Outline each uninfected red blood cell.
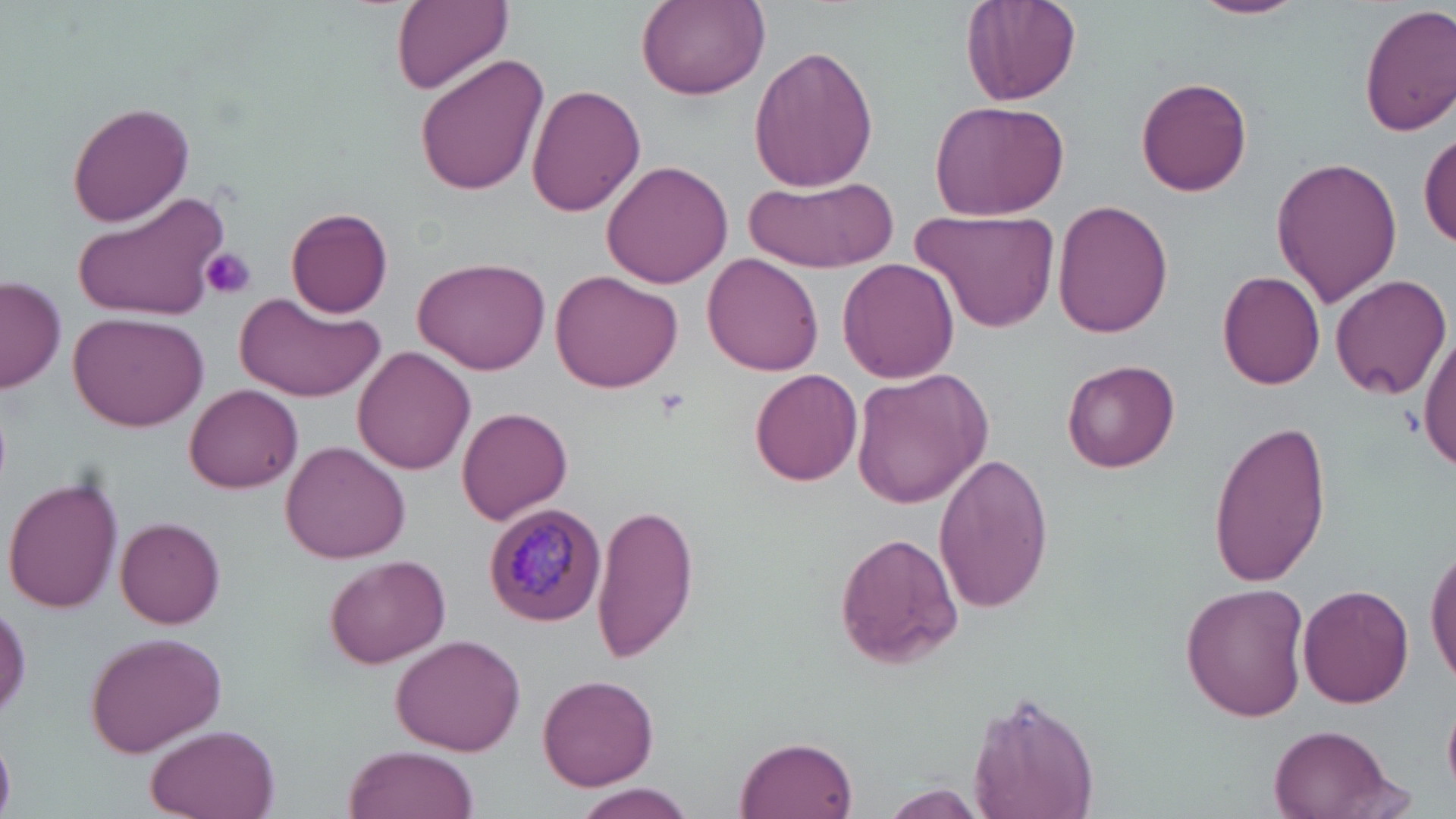

Approximate bounding boxes as (x1, y1, x2, y2) in pixels.
Uninfected red blood cells: (393, 0, 512, 92), (960, 0, 1082, 107), (1190, 0, 1307, 20), (635, 1, 769, 100), (1360, 4, 1456, 136), (747, 45, 879, 193), (414, 53, 549, 197), (1136, 77, 1253, 196), (527, 85, 646, 217), (927, 98, 1071, 221), (67, 102, 195, 227), (1418, 128, 1455, 250), (1271, 156, 1404, 308), (600, 158, 733, 290), (745, 174, 896, 273), (78, 190, 227, 321), (1054, 199, 1175, 338), (916, 207, 1060, 334), (284, 208, 393, 317), (703, 252, 824, 376), (415, 255, 551, 373), (838, 260, 960, 385), (550, 269, 683, 391), (1217, 271, 1326, 389), (1329, 272, 1452, 401), (0, 277, 65, 392), (240, 298, 384, 401), (66, 311, 208, 430), (1419, 330, 1456, 471), (354, 346, 475, 477), (1064, 359, 1180, 472), (751, 368, 862, 487), (853, 368, 990, 509), (185, 384, 303, 493), (458, 406, 571, 526), (1208, 417, 1331, 587), (281, 441, 410, 564), (935, 454, 1054, 613), (4, 475, 124, 615), (593, 504, 698, 659), (117, 515, 227, 628), (836, 533, 963, 665), (1427, 543, 1456, 688), (324, 554, 452, 669), (1182, 584, 1310, 723), (1296, 584, 1415, 709), (85, 629, 227, 758), (392, 633, 527, 755), (538, 674, 657, 791), (962, 688, 1100, 819), (140, 724, 279, 819), (1269, 728, 1396, 818), (737, 734, 860, 819), (344, 745, 479, 819), (570, 782, 698, 819), (883, 783, 988, 816).

Plasmodium malariae-infected red blood cell locations: (482, 501, 607, 627). Platelet locations: (200, 247, 256, 300). Slide-level diagnosis: Plasmodium malariae. Optical microscopy. Thin blood smear. Image is 1456×819 pixels. May-Grünwald-Giemsa-stained preparation. Single field of view. Captured at 1000x magnification.